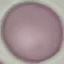

Malaria status: uninfected. Thin smear of blood. Cell patch, automatically extracted from a larger field of view and resized to 64 × 64 pixels. Photographed with a smartphone camera at the microscope eyepiece. Giemsa-stained preparation.